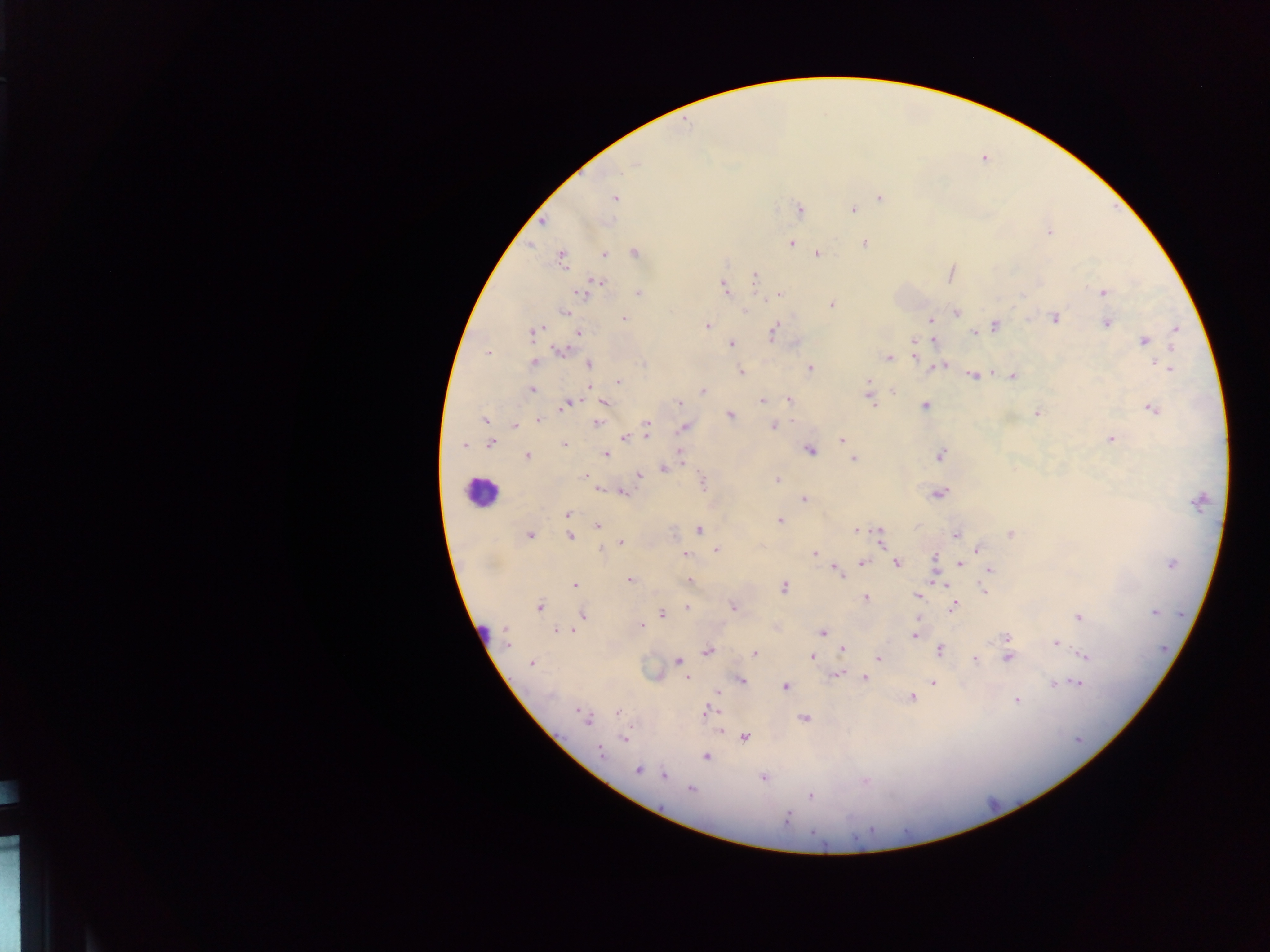

Approximate centers as {x, y} in pixels.
Summary:
  - Leukocyte locations: {482, 492}, {482, 631}
  - Plasmodium parasite locations: {635, 165}, {614, 198}, {880, 198}, {800, 209}, {853, 210}, {542, 221}, {1049, 232}, {865, 243}, {791, 244}, {635, 252}, {817, 253}, {605, 255}, {561, 258}, {951, 274}, {755, 278}, {589, 288}, {724, 288}, {1103, 292}, {638, 293}, {780, 295}, {832, 304}, {565, 311}, {745, 311}, {957, 312}, {1055, 318}, {625, 319}, {931, 320}, {1108, 323}, {995, 325}, {707, 326}, {1175, 329}, {773, 332}, {533, 333}, {579, 333}, {974, 333}, {933, 341}, {1143, 341}, {914, 342}, {732, 343}, {796, 343}, {560, 352}, {914, 352}, {487, 353}, {889, 358}, {535, 363}, {589, 364}, {644, 364}, {941, 365}, {1167, 366}, {935, 367}, {811, 368}, {741, 371}, {990, 373}, {973, 375}, {1012, 376}, {619, 382}, {868, 383}, {531, 389}, {869, 389}, {704, 390}, {893, 391}, {870, 397}, {789, 399}, {762, 401}, {680, 402}, {568, 403}, {604, 403}, {924, 406}, {1153, 408}, {1037, 413}, {730, 415}, {484, 420}, {539, 420}, {597, 423}, {647, 423}, {514, 426}, {774, 427}, {684, 428}, {647, 435}, {624, 437}, {1111, 439}, {842, 440}, {490, 444}, {464, 445}, {564, 445}, {810, 450}, {605, 454}, {680, 455}, {940, 455}, {527, 456}, {853, 459}, {664, 468}, {640, 476}, {584, 477}, {778, 479}, {703, 482}, {600, 490}, {623, 492}, {938, 493}, {804, 499}, {1199, 501}, {566, 514}, {780, 521}, {598, 525}, {699, 530}, {857, 530}, {878, 530}, {1011, 533}, {956, 535}, {530, 536}, {570, 536}, {881, 539}, {621, 542}, {600, 549}, {978, 549}, {717, 550}, {814, 553}, {684, 554}, {934, 559}, {862, 563}, {896, 563}, {960, 564}, {1171, 564}, {837, 570}, {990, 570}, {629, 580}, {690, 581}, {574, 586}, {783, 587}, {984, 590}, {918, 596}, {866, 598}, {732, 606}, {539, 607}, {687, 607}, {953, 608}, {1154, 612}, {661, 613}, {584, 615}, {1078, 617}, {642, 625}, {506, 629}, {575, 630}, {557, 631}, {822, 633}, {914, 635}, {1006, 637}, {1055, 643}, {508, 646}, {843, 649}, {940, 651}, {708, 652}, {755, 654}, {1085, 656}, {811, 657}, {879, 658}, {1008, 658}, {677, 660}, {975, 660}, {531, 664}, {837, 674}, {687, 678}, {864, 678}, {742, 681}, {933, 682}, {1054, 683}, {1078, 684}, {785, 686}, {717, 692}, {550, 697}, {911, 698}, {1017, 699}, {577, 711}, {707, 712}, {617, 713}, {582, 716}, {587, 719}, {805, 719}, {719, 731}, {744, 737}, {624, 738}, {602, 753}, {706, 757}, {638, 770}, {664, 775}, {763, 777}, {865, 781}, {691, 790}, {810, 795}, {787, 817}
  - Field of view: single
  - Capture: mobile-phone photograph through a microscope
  - Country: Ghana
  - Preparation: thick blood smear
  - Image size: 1270×952 pixels